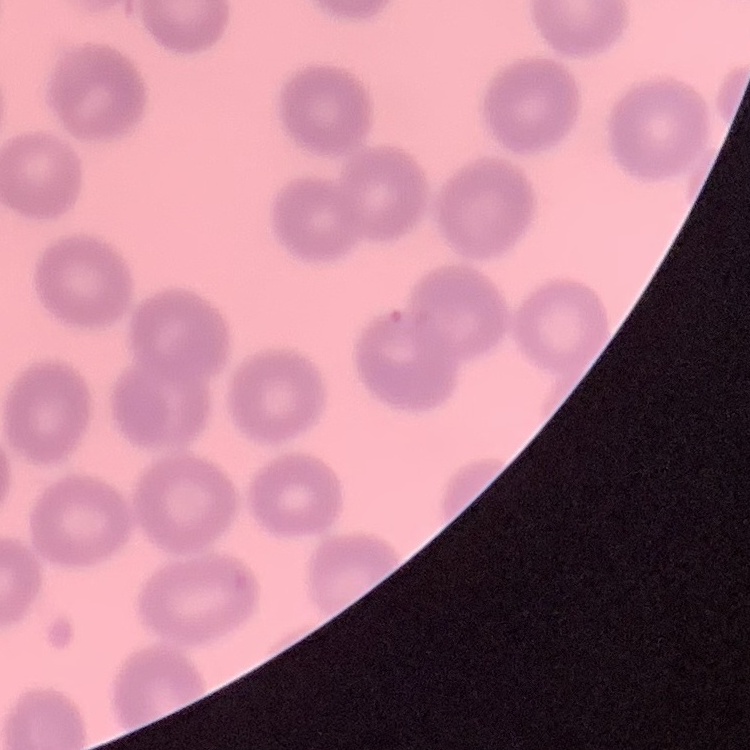

erythrocyte morphology = no rouleaux formation
stain = Field's or Giemsa
preparation = thin blood smear
image type = one tile cut from a larger photomicrograph